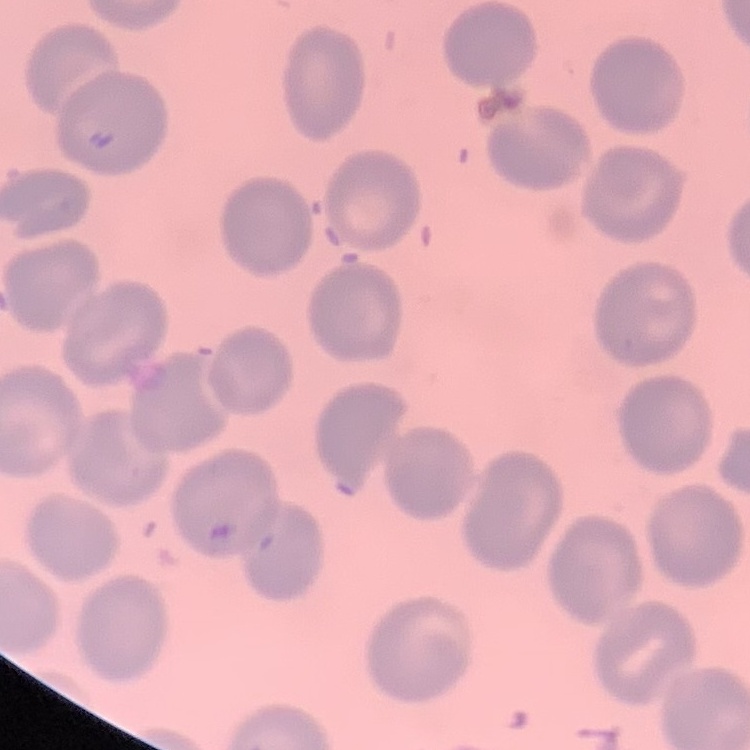

erythrocyte morphology = no rouleaux formation
preparation = thin blood film
image type = one tile cut from a larger photomicrograph
stain = Field's or Giemsa